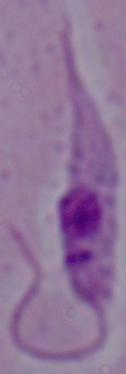

Summary:
  - Modality: micrograph
  - Magnification: 1000x
  - Identification: Leishmania